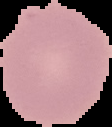 Image is 112×127 pixels. From a thin blood film. Malaria status: uninfected. The area outside the segmented cell region is set to black.